State which cell type is depicted.
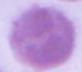
An erythrocyte.

Micrograph. 1000x magnification.